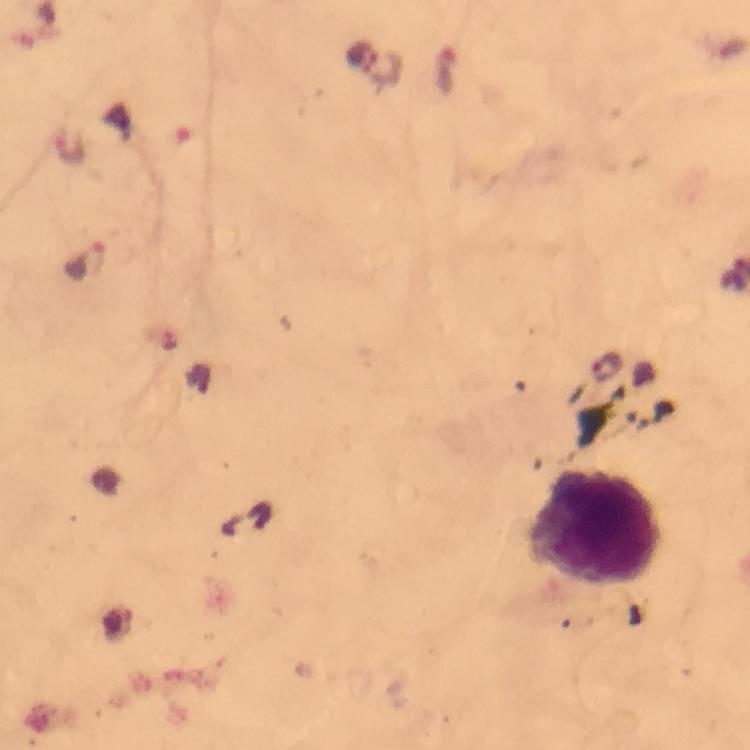
Approximate centers as {x, y} in pixels.
Summary:
  - Plasmodium parasite locations: {361, 54}, {383, 69}, {69, 147}, {86, 262}, {609, 369}
  - Leukocyte locations: {596, 528}
  - Preparation: thick blood smear
  - Stain: Giemsa
  - Context: from a malaria diagnostic workup
  - Image size: 750×750 pixels
  - Immersion oil: used
  - Capture: smartphone photograph through a microscope
  - Magnification: 100x
  - Cropped from: a single field of view